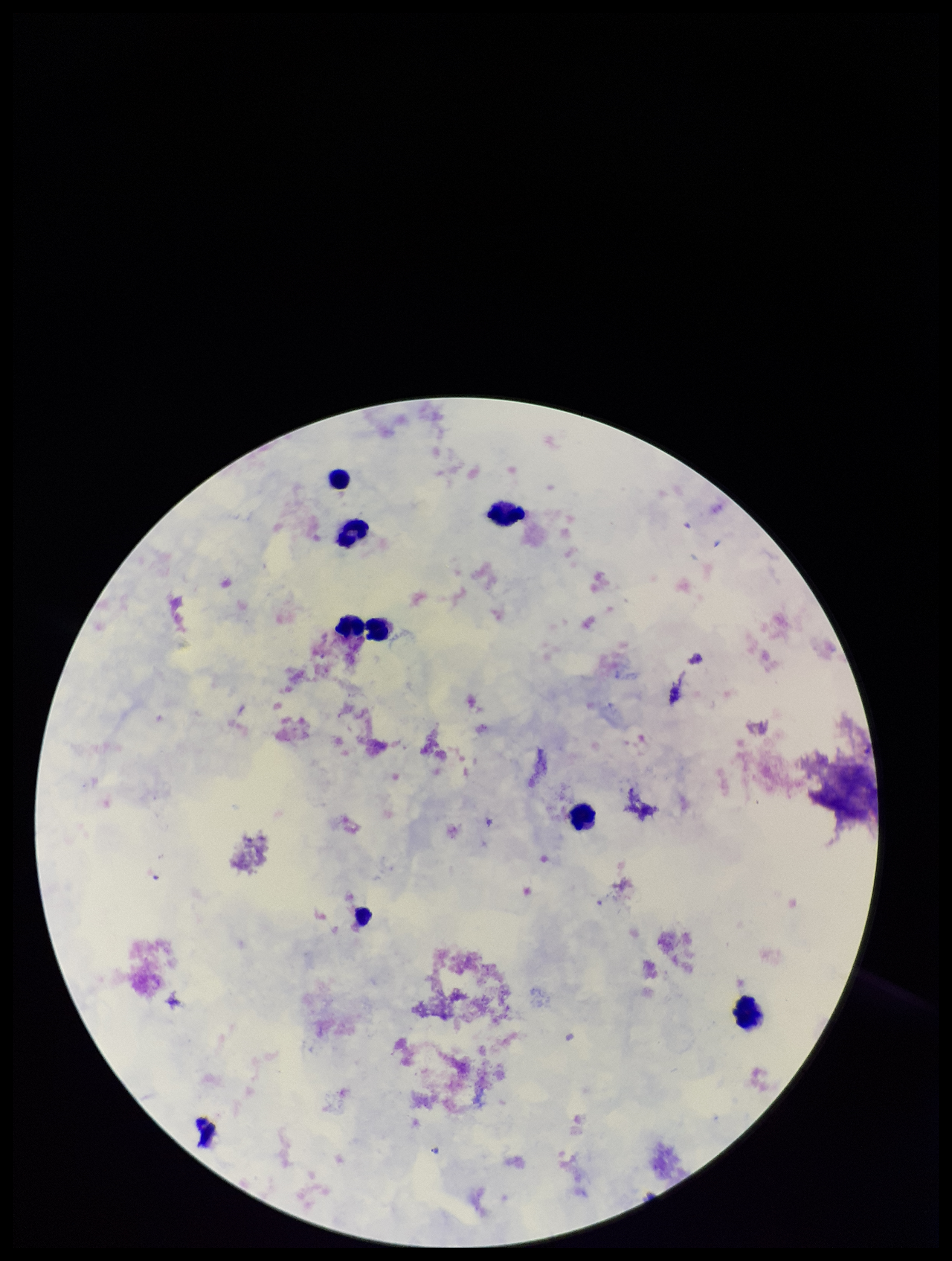 Photographed through the microscope eyepiece with a smartphone camera. Single field of view. Plasmodium parasites: none identified. Patient malaria status: negative. Preparation: thick smear. Leukocyte count: 7. Image is 952×1261 pixels. Giemsa stain. Parasite count: 0.